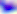

Summary:
  - Identification: Toxoplasma gondii
  - Modality: micrograph
  - Magnification: 400x